Assess this cell for malaria.
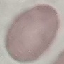
Uninfected.

Summary:
  - Image type: cell patch, automatically extracted from a larger field of view and resized to 64 × 64 pixels
  - Capture: smartphone camera at the microscope eyepiece
  - Preparation: thin smear
  - Stain: Giemsa